Name the parasite shown.
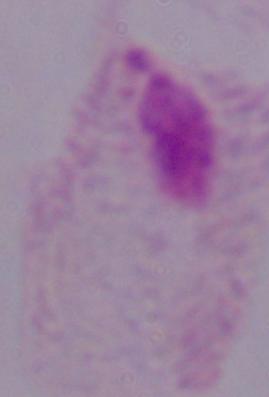

A trichomonad.

Photomicrograph. 1000x magnification.